Identify the preparation type.
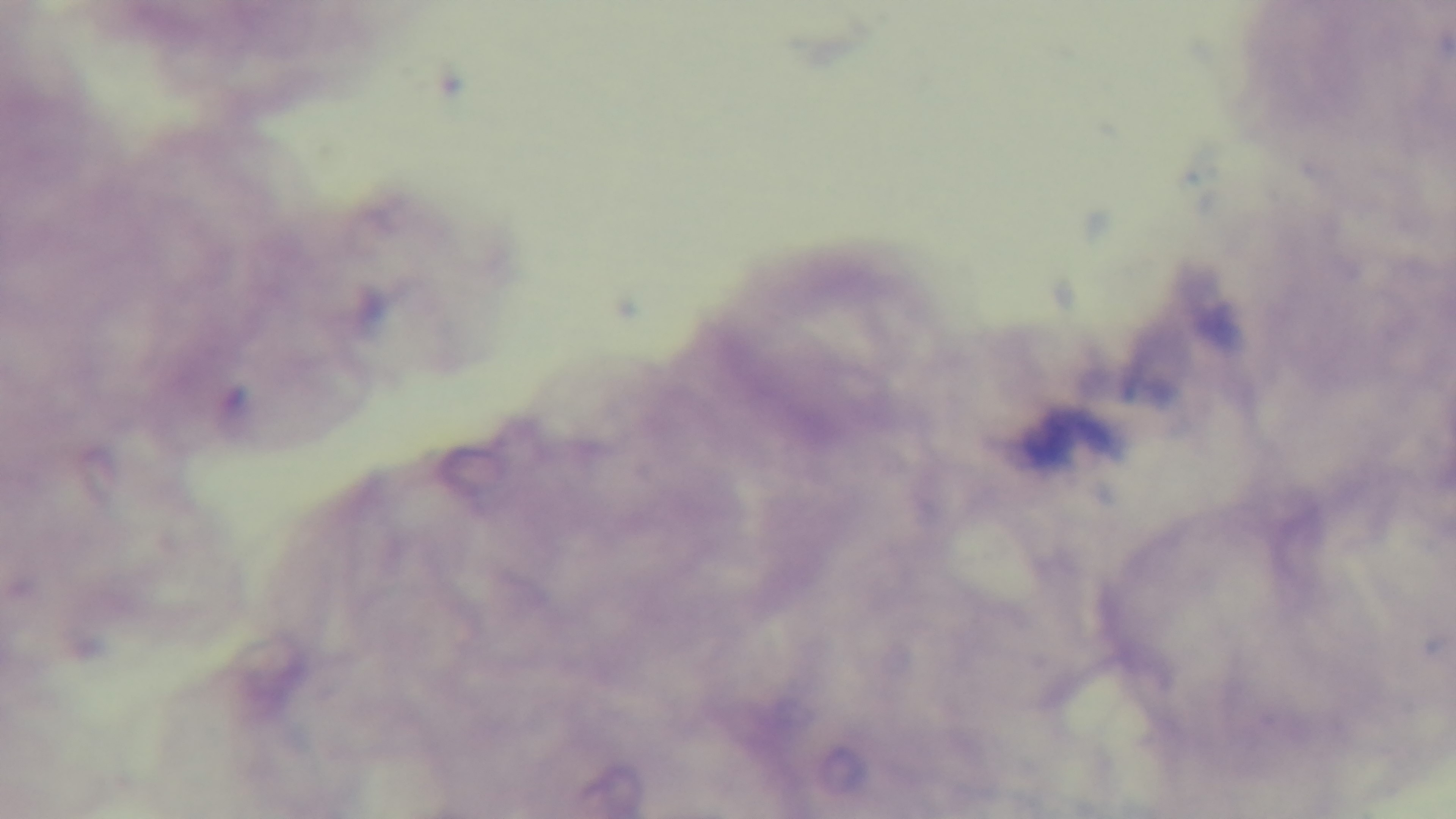

A thick smear.

Single field of view. Mounted 4K digital camera. Giemsa-stained. Oil-immersion objective, 100x. Malaria status: uninfected. Light microscopy.